Find each parasitized RBC.
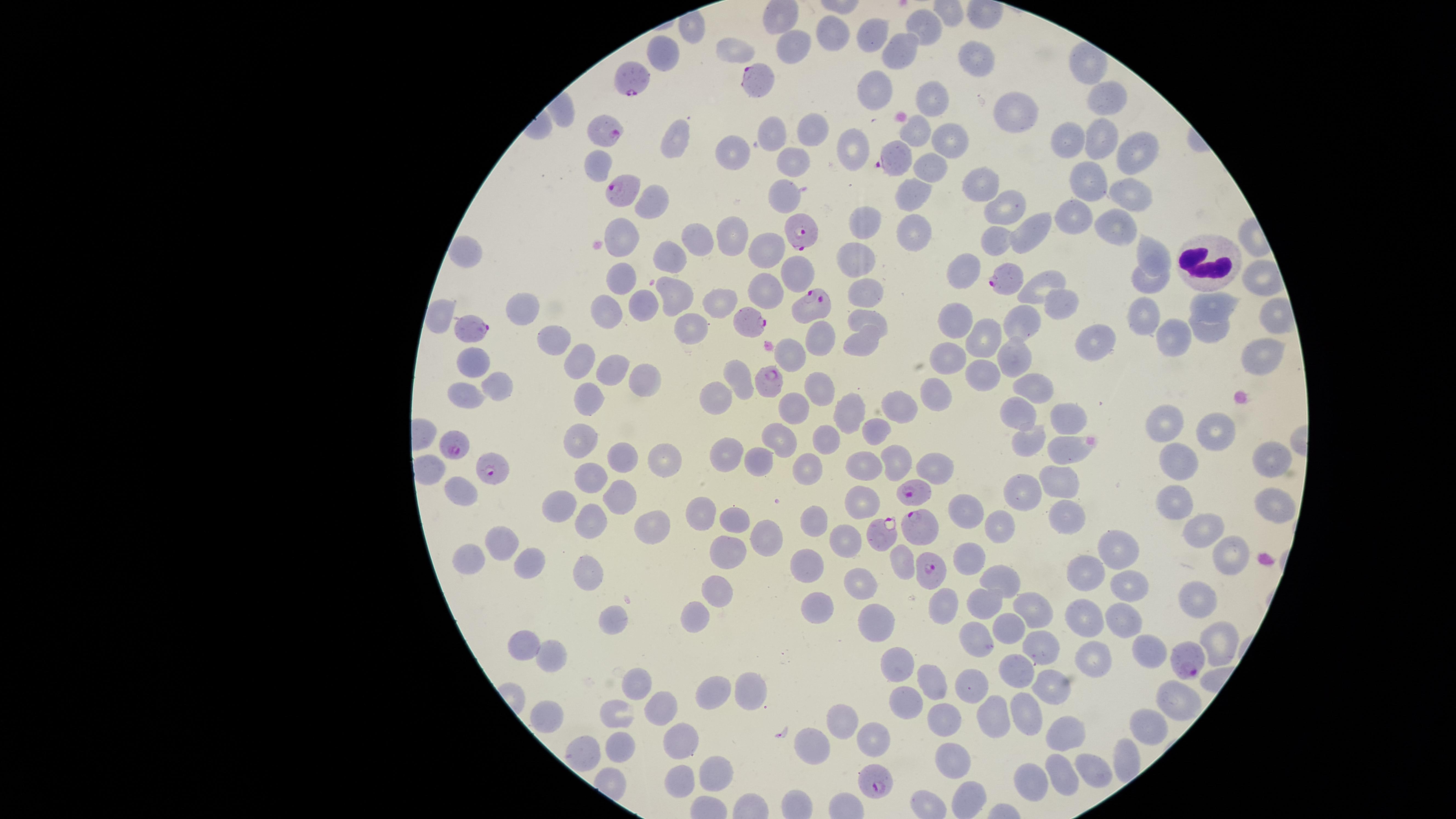
Approximate marker points, in pixels from the top-left corner.
Parasitized RBCs: (x=758, y=76), (x=633, y=78), (x=605, y=130), (x=894, y=157), (x=619, y=189), (x=799, y=229), (x=1007, y=280), (x=811, y=304), (x=749, y=322), (x=473, y=334), (x=770, y=383), (x=452, y=442), (x=495, y=470), (x=915, y=489), (x=919, y=525), (x=880, y=531), (x=929, y=570), (x=1189, y=659), (x=876, y=779).

uninfected RBCs = approximate marker points, in pixels from the top-left corner: (x=927, y=25), (x=875, y=30), (x=830, y=31), (x=795, y=44), (x=733, y=46), (x=903, y=46), (x=665, y=55), (x=973, y=56), (x=875, y=87), (x=1104, y=97), (x=937, y=98), (x=1015, y=111), (x=812, y=131), (x=773, y=134), (x=918, y=134), (x=678, y=136), (x=1067, y=137), (x=1100, y=140), (x=952, y=142), (x=856, y=147), (x=742, y=149), (x=1131, y=152), (x=791, y=161), (x=931, y=164), (x=1094, y=171), (x=981, y=181), (x=916, y=189), (x=1128, y=191), (x=782, y=196), (x=655, y=204), (x=1004, y=206), (x=1078, y=218), (x=1119, y=218), (x=869, y=221), (x=1032, y=225), (x=911, y=228), (x=740, y=230), (x=625, y=232), (x=698, y=239), (x=999, y=241), (x=767, y=247), (x=1146, y=254), (x=675, y=258), (x=470, y=259), (x=862, y=260), (x=967, y=270), (x=799, y=271), (x=1051, y=276), (x=625, y=283), (x=765, y=283), (x=1146, y=283), (x=866, y=287), (x=670, y=295), (x=1060, y=303), (x=1221, y=304), (x=636, y=306), (x=722, y=307), (x=606, y=310), (x=532, y=311), (x=869, y=318), (x=1146, y=318), (x=1023, y=321), (x=956, y=322), (x=1212, y=328), (x=696, y=331), (x=990, y=333), (x=822, y=339), (x=1097, y=340), (x=1174, y=342), (x=864, y=343), (x=562, y=345), (x=787, y=351), (x=1016, y=353), (x=946, y=358), (x=1255, y=359), (x=580, y=362), (x=475, y=364), (x=615, y=368), (x=642, y=377), (x=985, y=377), (x=739, y=380), (x=1043, y=382), (x=504, y=386), (x=815, y=387), (x=934, y=391), (x=468, y=394), (x=721, y=395), (x=586, y=403), (x=795, y=405), (x=856, y=409), (x=900, y=410), (x=1015, y=417), (x=1066, y=419), (x=1208, y=419), (x=1168, y=421), (x=882, y=432), (x=779, y=434), (x=1035, y=438), (x=831, y=440), (x=585, y=441), (x=1066, y=450), (x=731, y=456), (x=625, y=457), (x=901, y=459), (x=1188, y=459), (x=666, y=460), (x=1269, y=460), (x=762, y=463), (x=869, y=463), (x=811, y=465), (x=935, y=465), (x=594, y=478), (x=1056, y=482), (x=462, y=483), (x=1020, y=488), (x=859, y=495), (x=624, y=498), (x=1273, y=502), (x=1184, y=506), (x=565, y=508), (x=971, y=512), (x=821, y=513), (x=708, y=514), (x=1066, y=514), (x=592, y=517), (x=741, y=519), (x=653, y=521), (x=999, y=523), (x=1204, y=529), (x=767, y=533), (x=848, y=540), (x=1120, y=545), (x=510, y=546), (x=727, y=548), (x=1224, y=550), (x=977, y=551), (x=904, y=557), (x=814, y=558), (x=471, y=559), (x=535, y=560), (x=586, y=568), (x=1084, y=570), (x=1003, y=579), (x=861, y=580), (x=1131, y=581), (x=718, y=586), (x=1200, y=597), (x=813, y=599), (x=989, y=601), (x=946, y=602), (x=1030, y=606), (x=702, y=615), (x=1086, y=616), (x=1122, y=616), (x=875, y=618), (x=1011, y=624), (x=610, y=625), (x=1225, y=631), (x=979, y=640), (x=1041, y=642), (x=527, y=645), (x=1138, y=649), (x=1092, y=650), (x=552, y=655), (x=900, y=669), (x=1015, y=676), (x=1056, y=679), (x=643, y=680), (x=752, y=685), (x=934, y=685), (x=975, y=686), (x=720, y=690), (x=1180, y=700), (x=669, y=704), (x=909, y=704), (x=547, y=715), (x=616, y=715), (x=994, y=716), (x=1031, y=716), (x=842, y=724), (x=947, y=724), (x=1151, y=724), (x=684, y=735), (x=877, y=739), (x=1065, y=739), (x=816, y=745), (x=618, y=749), (x=1123, y=753), (x=955, y=763), (x=1097, y=770), (x=719, y=772), (x=679, y=776), (x=1065, y=780), (x=1031, y=783)
species = Plasmodium falciparum
capture = smartphone photograph through the microscope eyepiece
image size = 1456×819 pixels
stain = Giemsa
field of view = single
WBCs = approximate marker points, in pixels from the top-left corner: (x=1203, y=260)
visible region = circular
preparation = thin blood smear